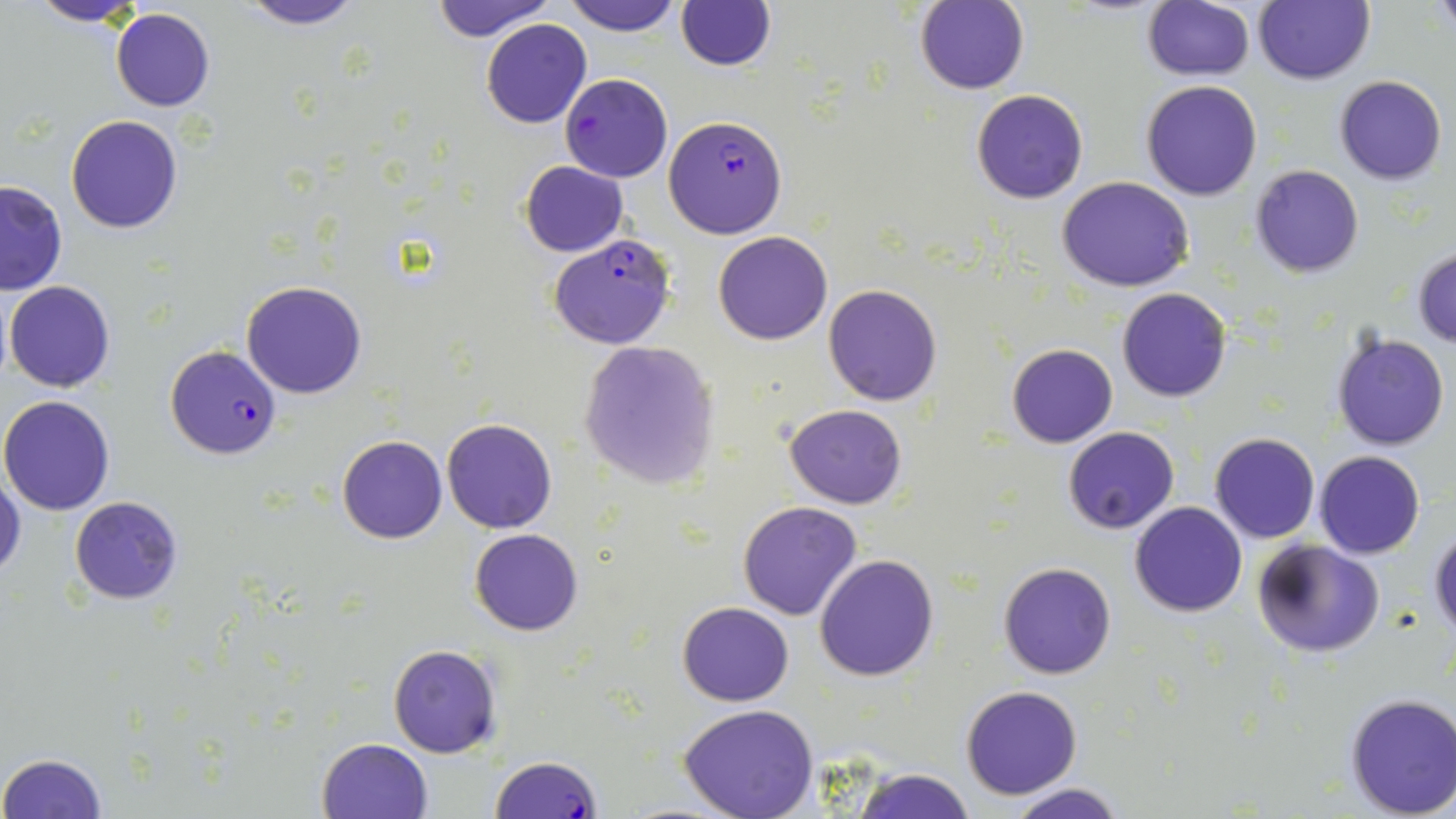
Approximate bounding boxes as (x1, y1, x2, y2) in pixels. Plasmodium falciparum-infected red blood cell locations: (560, 74, 672, 183), (662, 114, 788, 239), (547, 233, 676, 350), (165, 346, 281, 460), (489, 754, 604, 819). Uninfected red blood cell locations: (24, 0, 149, 27), (232, 0, 370, 29), (430, 0, 557, 42), (563, 0, 682, 36), (1255, 0, 1375, 85), (675, 1, 774, 71), (916, 2, 1030, 95), (1143, 2, 1256, 81), (110, 9, 216, 111), (480, 18, 591, 128), (1334, 75, 1446, 186), (1142, 80, 1263, 201), (971, 89, 1088, 204), (65, 115, 185, 234), (520, 159, 629, 256), (1250, 165, 1363, 278), (1058, 176, 1196, 292), (0, 179, 68, 297), (713, 231, 833, 344), (1413, 247, 1456, 347), (4, 280, 115, 393), (241, 281, 368, 399), (823, 283, 943, 406), (1116, 287, 1232, 402), (1332, 332, 1450, 450), (577, 341, 720, 490), (1006, 344, 1117, 447), (1, 395, 117, 514), (784, 403, 908, 509), (441, 417, 558, 534), (1063, 427, 1179, 534), (1209, 432, 1321, 543), (336, 434, 448, 543), (1314, 450, 1425, 559), (0, 475, 26, 582), (69, 497, 183, 604), (737, 500, 864, 620), (1130, 502, 1247, 618), (469, 528, 585, 635), (1429, 530, 1456, 639), (1251, 539, 1384, 660), (815, 554, 939, 682), (998, 563, 1116, 680), (678, 601, 794, 706), (387, 643, 502, 758), (960, 685, 1084, 800), (1344, 692, 1456, 818), (678, 706, 821, 819), (317, 737, 434, 819), (0, 753, 109, 819), (853, 768, 976, 819), (1002, 782, 1131, 819). Slide-level diagnosis: Plasmodium falciparum. May-Grünwald-Giemsa stain. Thin blood film. Captured at 1000x magnification. Optical microscopy. Image is 1456×819 pixels. One field of a larger specimen.